Identify the parasite.
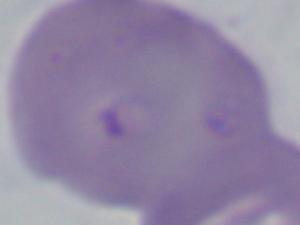

This is Babesia.

Summary:
  - Modality: micrograph
  - Magnification: 1000x